Outline each Plasmodium falciparum-infected red blood cell.
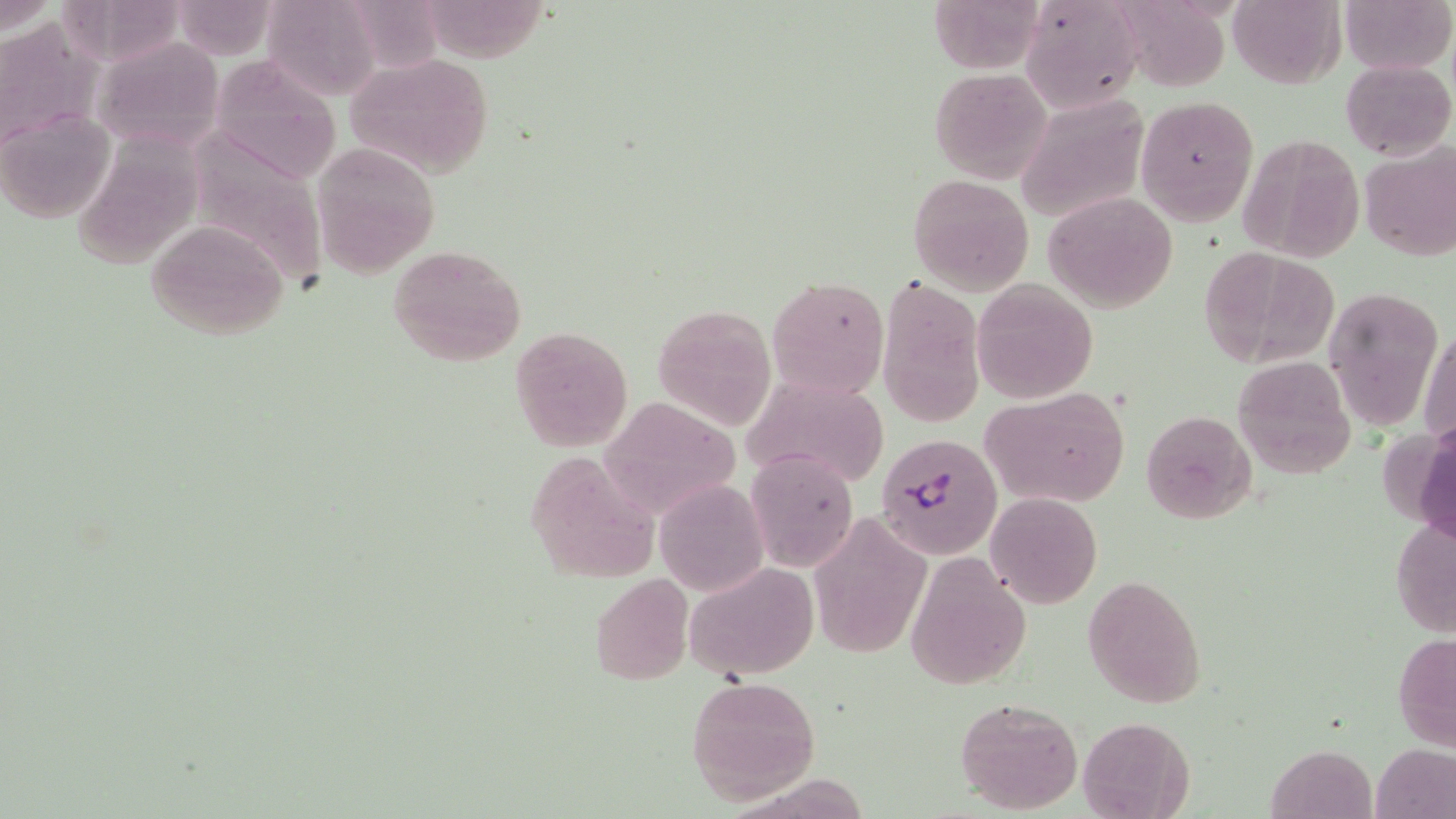

Approximate bounding boxes as [x1, y1, x2, y2] in pixels.
Plasmodium falciparum-infected red blood cells: [876, 433, 1002, 559].

{
  "slide_level_diagnosis": "Plasmodium falciparum",
  "modality": "light microscopy",
  "uninfected_red_blood_cell_locations": "approximate bounding boxes as [x1, y1, x2, y2] in pixels: [59, 0, 189, 67], [1228, 0, 1343, 88], [1340, 0, 1453, 74], [1, 1, 58, 34], [1019, 1, 1141, 111], [169, 2, 281, 60], [259, 2, 381, 100], [0, 19, 100, 155], [94, 35, 225, 154], [221, 52, 342, 177], [344, 55, 496, 179], [1341, 58, 1454, 161], [929, 68, 1050, 184], [1015, 93, 1150, 226], [1137, 95, 1257, 227], [0, 108, 115, 224], [172, 126, 333, 293], [1237, 134, 1365, 263], [310, 141, 440, 279], [1360, 141, 1456, 262], [907, 173, 1035, 295], [1044, 191, 1177, 312], [144, 220, 288, 341], [387, 244, 527, 367], [1203, 248, 1340, 368], [879, 274, 985, 429], [768, 275, 889, 400], [972, 280, 1097, 403], [1323, 285, 1447, 430], [653, 305, 777, 429], [1419, 323, 1455, 455], [508, 325, 632, 451], [737, 356, 893, 484], [1235, 356, 1358, 480], [982, 390, 1132, 511], [613, 401, 745, 519], [1141, 410, 1256, 524], [746, 447, 859, 573], [524, 449, 658, 586], [654, 478, 769, 598], [985, 493, 1102, 607], [1390, 508, 1456, 645], [815, 515, 929, 666], [905, 549, 1032, 691], [685, 563, 818, 680], [1083, 573, 1206, 708], [588, 574, 694, 685], [1393, 632, 1456, 751], [685, 675, 822, 804], [954, 698, 1083, 814], [1078, 716, 1193, 817], [1374, 742, 1456, 818], [1268, 745, 1378, 819]",
  "stain": "May-Grünwald-Giemsa",
  "preparation": "thin blood smear",
  "image_size": "1456×819 pixels",
  "field_of_view": "one of a larger specimen",
  "magnification": "1000x"
}